State the preparation type.
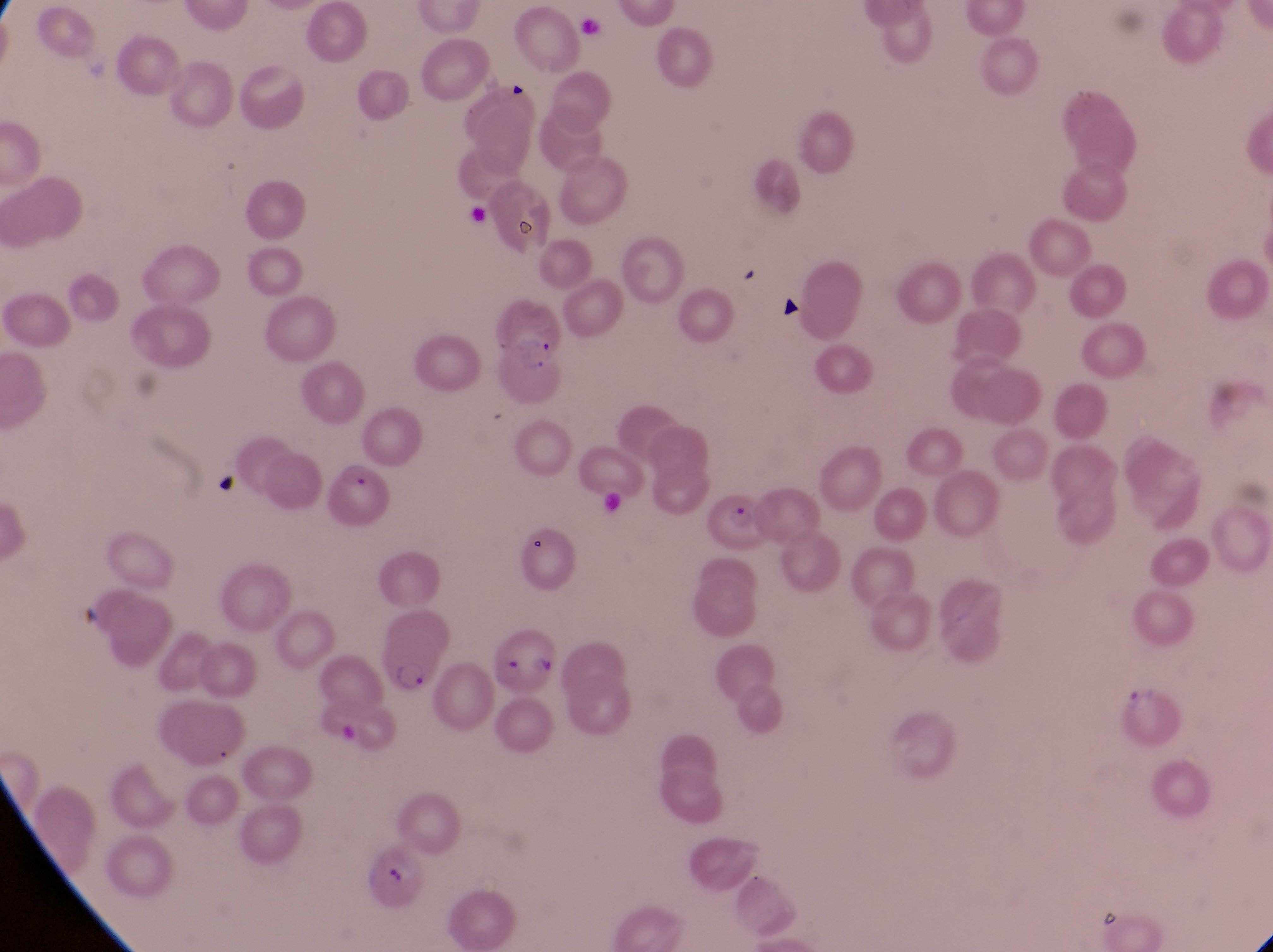
Thin blood film.

Approximate bounding boxes as {left, top, right, bottom} in pixels.
Summary:
  - Parasitised red blood cell locations: {497, 330, 564, 412}, {327, 455, 394, 535}, {709, 487, 769, 554}, {486, 617, 564, 702}, {377, 624, 446, 702}, {357, 846, 428, 913}
  - Field of view: single
  - Capture: smartphone photograph through the eyepiece of an Olympus CX-23 microscope
  - Country: Uganda
  - Magnification: 1000x
  - Image size: 1273×952 pixels